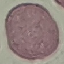
Summary:
  - Result: no malaria parasites detected
  - Image type: automatically extracted cell patch, resized to 64 × 64 pixels
  - Preparation: thin smear
  - Stain: Giemsa
  - Capture: smartphone camera at the microscope eyepiece